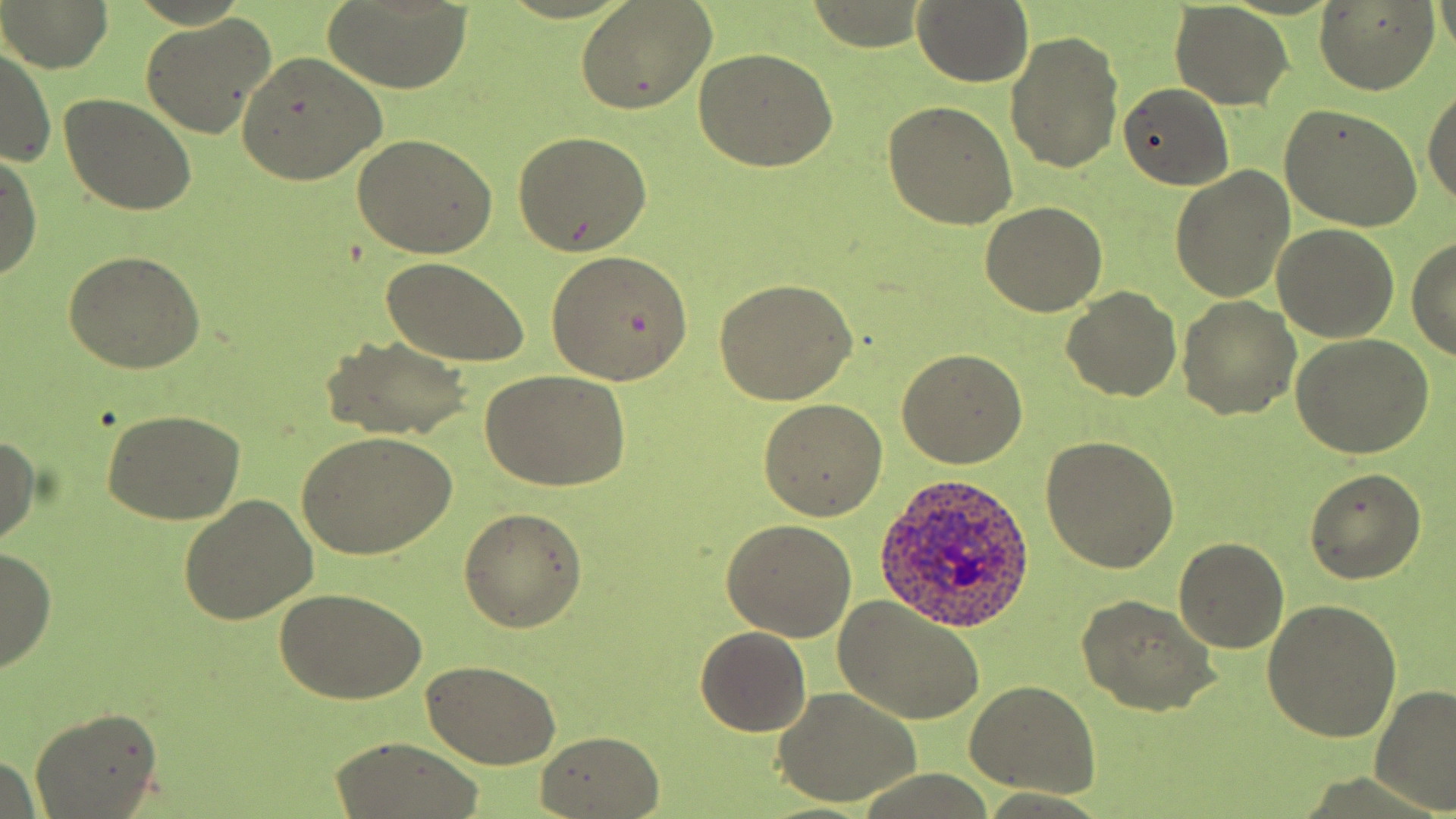 Approximate bounding boxes as [x1, y1, x2, y2] in pixels. Uninfected red blood cell locations: [912, 0, 1036, 87], [1436, 0, 1455, 63], [3, 1, 113, 73], [323, 1, 470, 96], [1312, 1, 1441, 96], [576, 4, 715, 114], [1171, 4, 1293, 109], [140, 13, 276, 140], [1006, 30, 1125, 174], [1, 46, 56, 165], [695, 47, 839, 173], [237, 51, 387, 185], [1117, 82, 1234, 189], [1422, 83, 1456, 214], [58, 93, 196, 216], [884, 102, 1018, 229], [1280, 105, 1425, 229], [512, 130, 652, 255], [352, 135, 499, 260], [0, 150, 42, 283], [1170, 168, 1295, 304], [980, 201, 1108, 316], [1272, 225, 1400, 343], [1406, 233, 1456, 363], [545, 249, 694, 384], [64, 252, 206, 373], [380, 255, 528, 366], [715, 278, 858, 405], [1062, 287, 1182, 401], [1178, 296, 1301, 420], [323, 334, 475, 440], [1291, 336, 1433, 459], [896, 348, 1027, 468], [479, 370, 633, 493], [760, 400, 889, 520], [100, 409, 244, 526], [295, 431, 459, 558], [0, 433, 42, 547], [1044, 435, 1180, 574], [1305, 467, 1425, 584], [178, 495, 316, 627], [458, 507, 586, 632], [720, 519, 858, 642], [1175, 539, 1287, 654], [0, 548, 57, 672], [274, 588, 428, 704], [1079, 595, 1217, 716], [832, 596, 987, 725], [1265, 598, 1404, 743], [696, 624, 811, 736], [422, 659, 559, 768], [965, 681, 1102, 798], [1371, 687, 1455, 810], [773, 688, 925, 806], [30, 709, 162, 819], [536, 729, 665, 818], [330, 737, 486, 819], [0, 750, 44, 817]. Plasmodium ovale-infected red blood cell locations: [873, 474, 1036, 632]. Slide-level diagnosis: Plasmodium ovale. Image is 1456×819 pixels. Light microscopy. May-Grünwald-Giemsa-stained preparation. Thin blood smear. Single field of view. Captured at 1000x magnification.